Give a bounding box for every malaria parasite, every leukocyte, and every artifact (stain precipitate or debris).
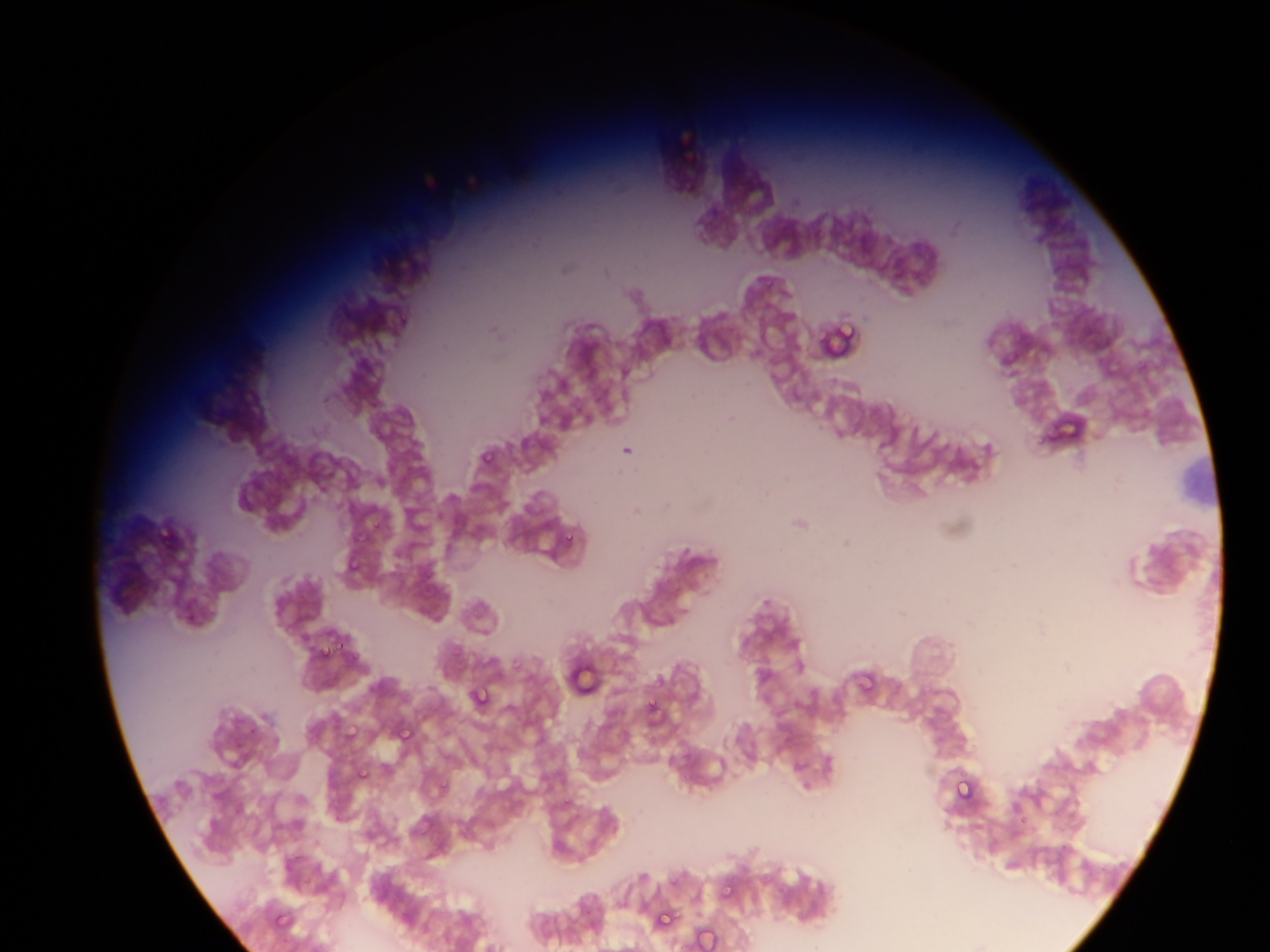

Approximate bounding boxes as left top right bottom in pixels.
Malaria parasites: 832 310 862 334; 1055 418 1088 432; 476 458 492 468; 369 515 390 540; 561 520 577 543; 340 554 362 568; 331 634 349 658; 314 644 325 656; 854 671 871 693; 467 684 494 713; 643 695 668 723; 342 720 358 742; 394 721 417 750; 349 770 363 780; 954 779 976 802; 719 887 730 894; 657 911 669 927; 695 924 719 952.
No leukocytes observed.

Summary:
  - Image size: 1270×952 pixels
  - Capture: mobile-phone photograph through a microscope
  - Preparation: thin blood smear
  - Country: Ghana
  - Field of view: single